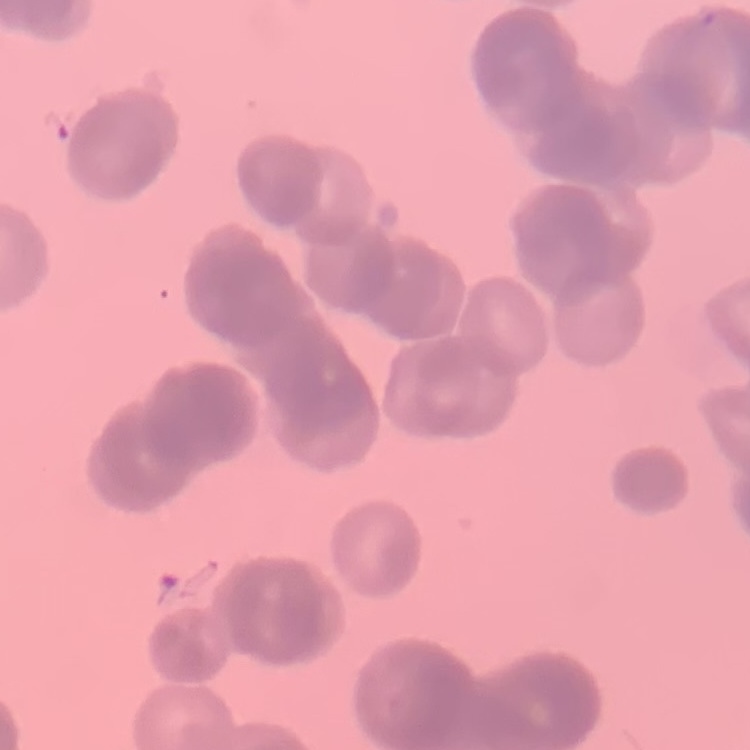
red blood cell morphology = rouleaux formation
image type = one tile cut from a larger photomicrograph
preparation = thin peripheral smear
stain = Field's or Giemsa